Point out each malaria parasite.
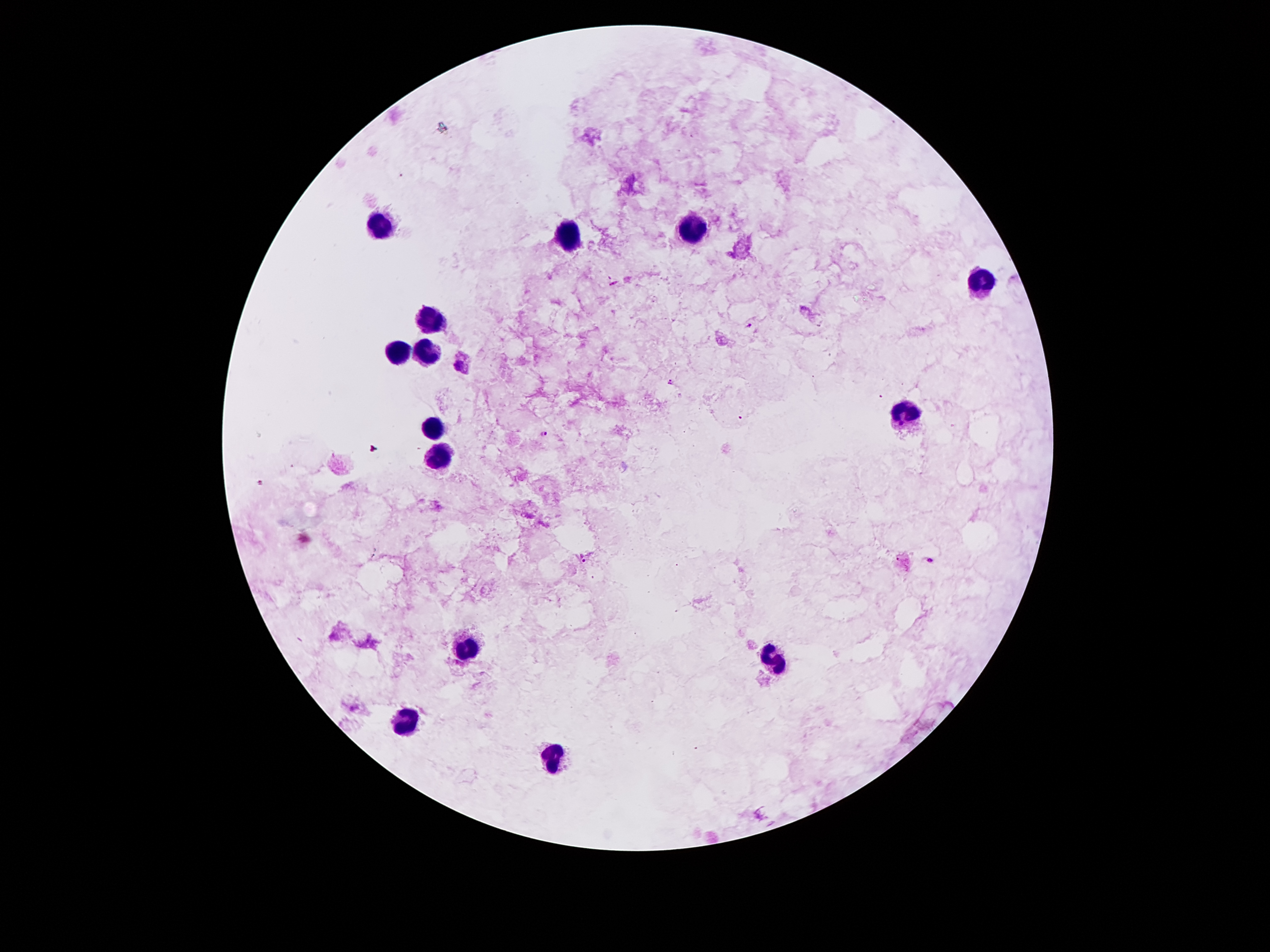
Approximate centers as (x, y) in pixels.
Malaria parasites: (748, 326), (458, 365), (671, 382), (544, 435), (583, 558), (931, 560).

{
  "stain": "Giemsa",
  "leukocyte_locations": "approximate centers as (x, y) in pixels: (379, 222), (689, 228), (567, 236), (981, 282), (431, 320), (393, 352), (425, 354), (909, 410), (433, 427), (441, 455), (463, 647), (775, 657), (405, 724), (551, 758)",
  "patient_malaria_status": "infected with Plasmodium falciparum",
  "preparation": "thick blood smear",
  "field_of_view": "single",
  "capture": "smartphone camera through the microscope eyepiece",
  "image_size": "1270×952 pixels",
  "magnification": "100x"
}